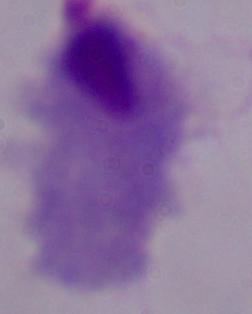
Summary:
  - Magnification: 1000x
  - Modality: photomicrograph
  - Identification: trichomonad